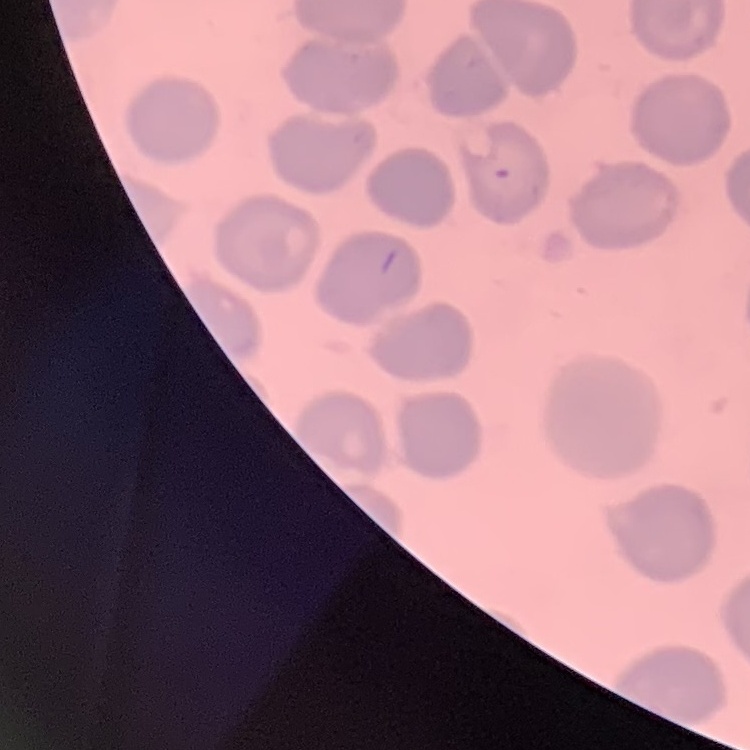
red blood cell morphology = no rouleaux formation
stain = Field's or Giemsa
image type = one tile cut from a larger photomicrograph
preparation = thin blood smear